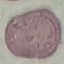 Result: negative for malaria parasites. Giemsa stain. Automatically extracted cell patch, resized to 64 × 64 pixels. Photographed with a smartphone camera at the microscope eyepiece. Thin blood smear.